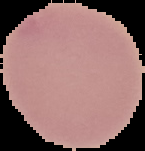
preparation = thin blood smear
image size = 145×151 pixels
image type = segmented cell region on a black background
result = no malaria parasites detected